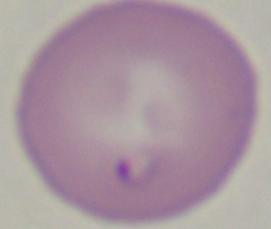

magnification = 1000x
identification = Babesia
modality = photomicrograph